State which parasite is depicted.
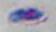

Toxoplasma gondii.

Micrograph. Captured at 1000x magnification.